Comment on the morphology of the erythrocytes.
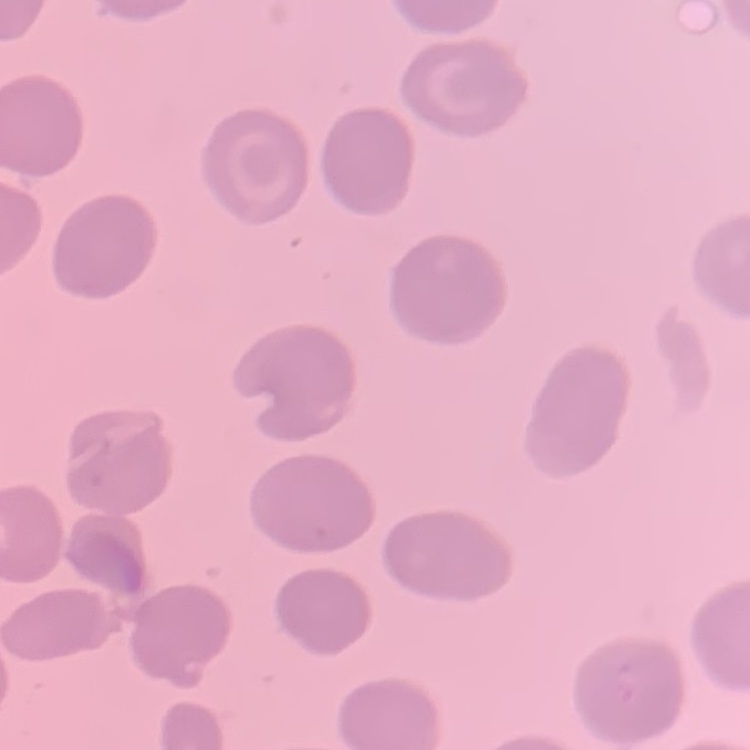

They show no rouleaux formation.

Summary:
  - Image type: one tile cut from a larger photomicrograph
  - Preparation: thin blood smear
  - Stain: Field's or Giemsa